Comment on the morphology of the erythrocytes.
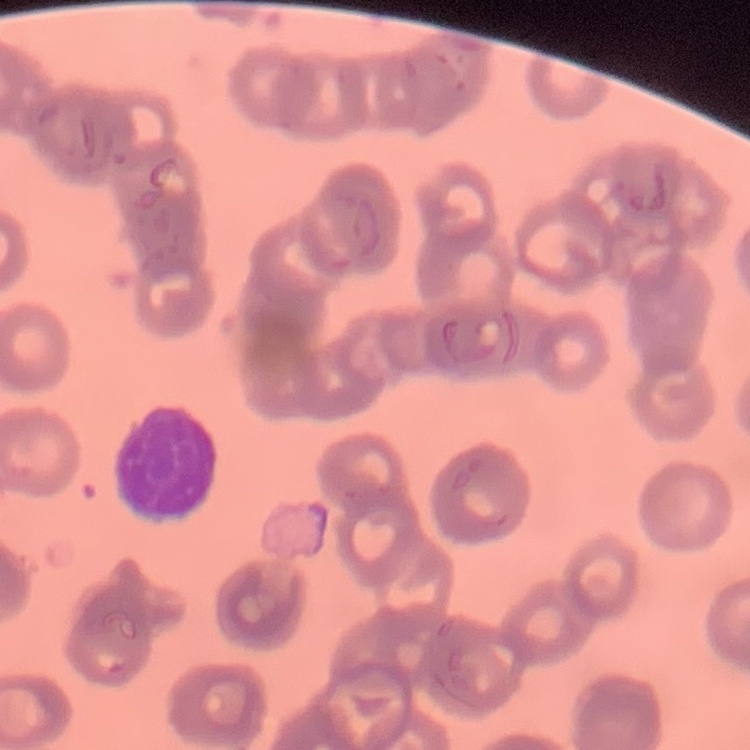
Rouleaux formation.

preparation: thin peripheral smear
stain: Field's or Giemsa
image_type: square crop of a larger photomicrograph